Locate every blood parasite and identify its species.
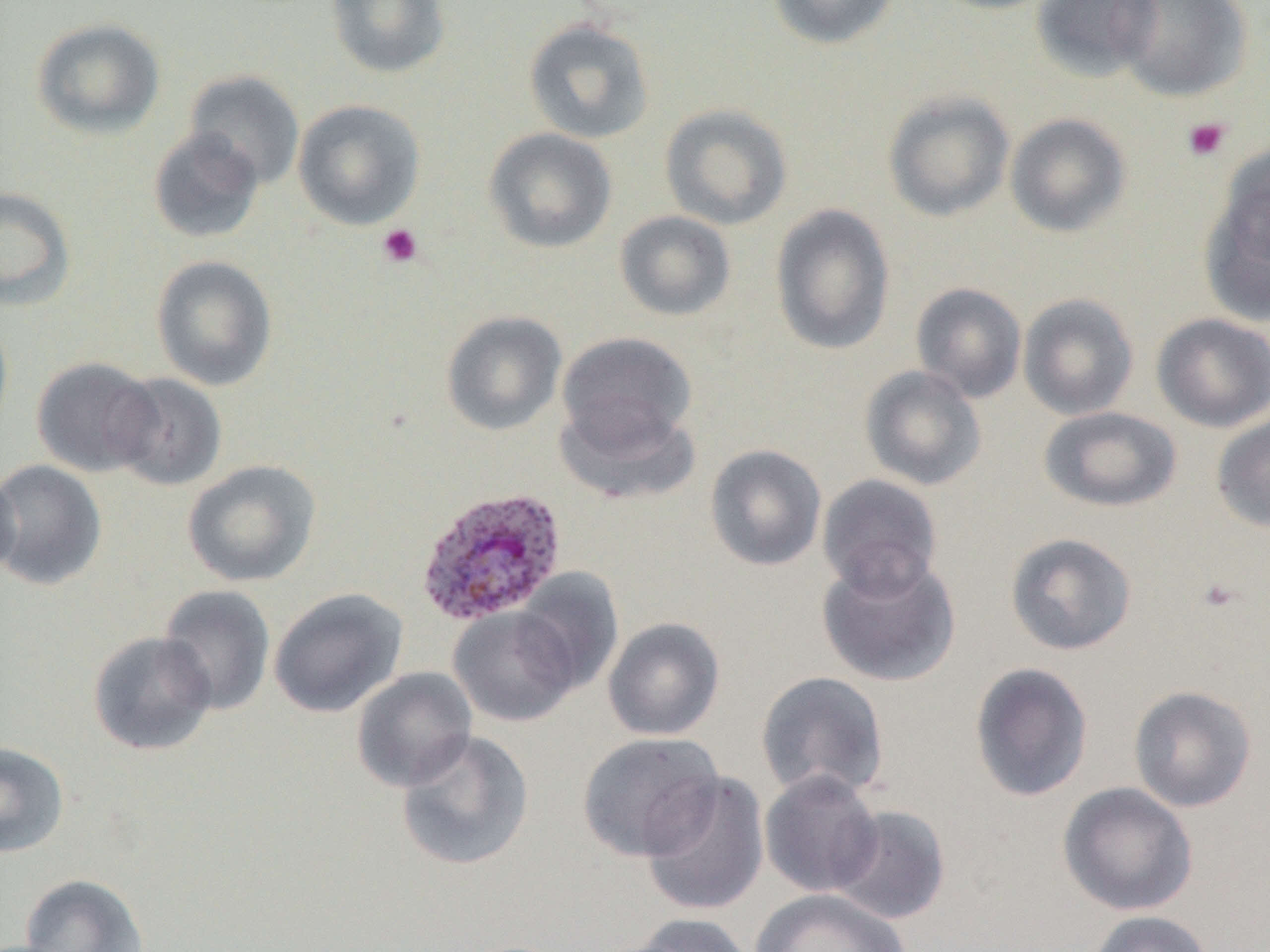
Approximate bounding boxes as (x1, y1, x2, y2) in pixels.
Plasmodium ovale-infected red blood cells: (414, 485, 568, 627).
No Plasmodium falciparum, Plasmodium malariae, Plasmodium vivax, Babesia divergens, or Trypanosoma brucei observed.

{
  "slide_level_diagnosis": "Plasmodium ovale",
  "preparation": "thin blood smear",
  "platelet_locations": "approximate bounding boxes as (x1, y1, x2, y2) in pixels: (1181, 116, 1232, 162), (377, 223, 423, 268), (1195, 576, 1242, 615)",
  "image_size": "1270×952 pixels",
  "field_of_view": "one of a larger specimen",
  "modality": "light microscopy",
  "magnification": "1000x",
  "uninfected_red_blood_cell_locations": "approximate bounding boxes as (x1, y1, x2, y2) in pixels: (325, 0, 451, 79), (767, 0, 899, 50), (928, 0, 1061, 14), (1031, 0, 1162, 81), (1113, 0, 1254, 102), (31, 18, 165, 139), (523, 18, 655, 144), (183, 70, 305, 190), (883, 91, 1015, 222), (293, 99, 425, 230), (660, 103, 793, 229), (1005, 113, 1132, 238), (147, 128, 265, 244), (483, 128, 618, 254), (1200, 170, 1270, 326), (0, 186, 76, 311), (770, 203, 896, 356), (614, 210, 736, 322), (150, 255, 278, 391), (910, 282, 1027, 403), (1018, 292, 1139, 420), (0, 311, 14, 446), (441, 311, 567, 436), (1151, 313, 1270, 432), (557, 331, 697, 454), (32, 356, 163, 477), (859, 365, 987, 491), (109, 372, 228, 492), (555, 399, 702, 505), (1038, 406, 1182, 512), (1211, 412, 1270, 532), (704, 444, 827, 571), (0, 459, 108, 591), (182, 459, 321, 587), (0, 466, 21, 581), (817, 473, 944, 599), (1004, 532, 1138, 656), (817, 553, 961, 687), (513, 568, 625, 694), (157, 584, 276, 717), (268, 587, 408, 718), (449, 606, 581, 727), (603, 617, 725, 740), (87, 630, 217, 756), (969, 662, 1094, 802), (351, 667, 477, 792), (756, 670, 890, 801), (1128, 685, 1258, 812), (395, 729, 535, 872), (576, 732, 724, 862), (0, 741, 70, 857), (759, 769, 884, 897), (640, 771, 770, 917), (1057, 782, 1198, 916), (829, 804, 951, 925), (18, 873, 149, 952), (751, 888, 910, 952), (1084, 910, 1216, 952), (623, 913, 758, 952)"
}